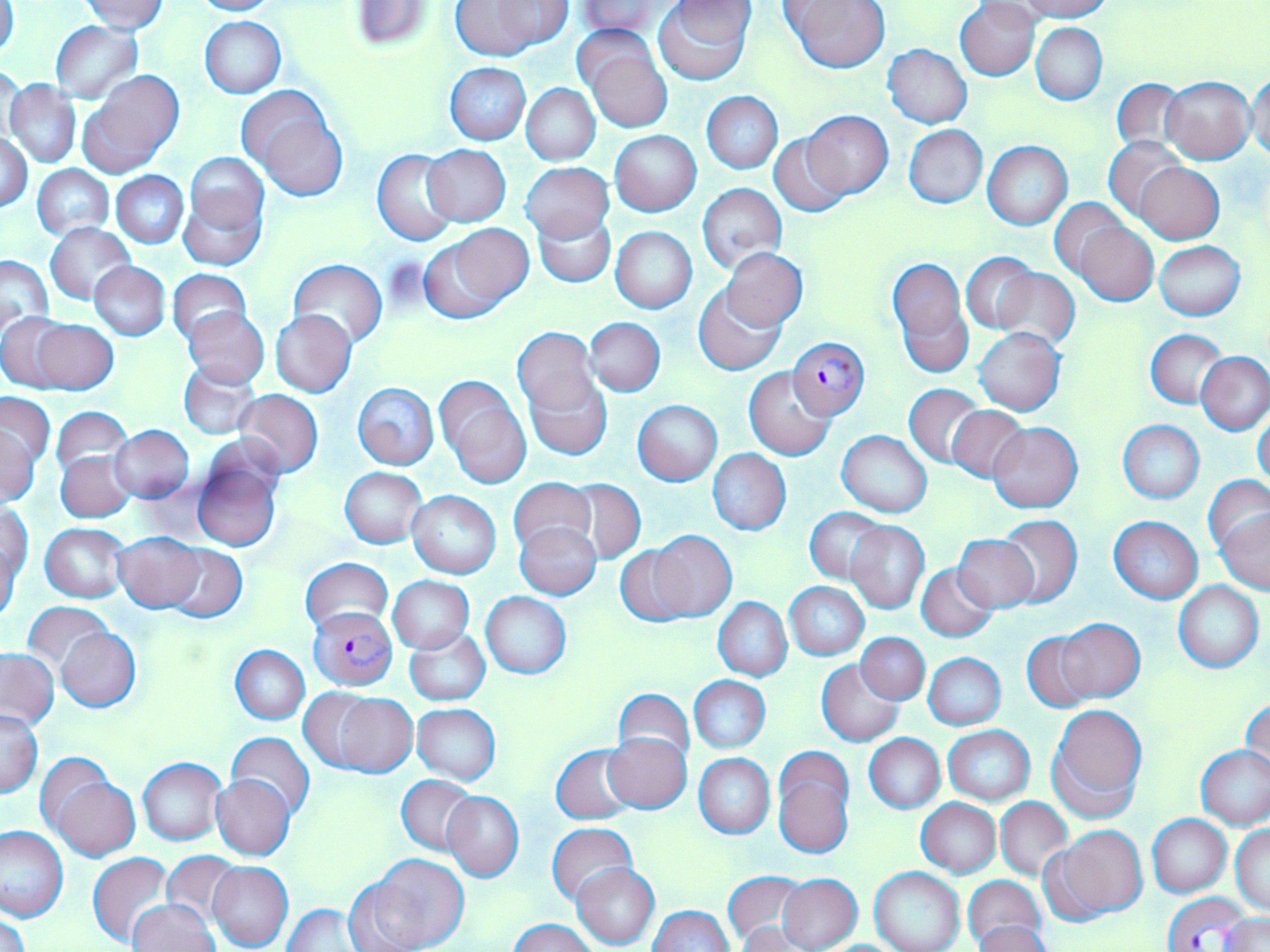
Summary:
  - Coordinate format: approximate bounding boxes as (x1, y1, x2, y2) in pixels
  - Uninfected red blood cell locations: (187, 0, 278, 16), (447, 0, 570, 60), (575, 0, 668, 38), (654, 0, 755, 86), (781, 0, 890, 72), (1017, 0, 1112, 21), (81, 1, 169, 35), (349, 1, 436, 50), (0, 2, 19, 62), (955, 2, 1040, 81), (199, 16, 286, 98), (51, 21, 142, 102), (1031, 22, 1107, 104), (583, 39, 675, 134), (883, 45, 971, 128), (445, 63, 531, 145), (1, 64, 25, 147), (78, 70, 183, 176), (1247, 72, 1270, 160), (1164, 76, 1253, 164), (1110, 77, 1188, 158), (5, 80, 82, 168), (520, 83, 600, 164), (237, 87, 344, 194), (702, 92, 782, 174), (803, 111, 893, 198), (904, 125, 988, 208), (610, 131, 701, 216), (1, 132, 32, 212), (769, 133, 854, 217), (904, 133, 1070, 216), (1105, 138, 1187, 223), (983, 142, 1071, 229), (422, 144, 511, 227), (373, 148, 460, 246), (185, 152, 268, 233), (521, 162, 613, 242), (1135, 162, 1223, 243), (32, 164, 115, 239), (112, 171, 188, 248), (698, 183, 786, 274), (178, 185, 266, 272), (1051, 198, 1133, 285), (534, 212, 614, 287), (1073, 219, 1158, 306), (45, 222, 136, 306), (419, 226, 532, 324), (611, 226, 698, 313), (1155, 241, 1246, 320), (720, 248, 807, 330), (962, 252, 1039, 333), (0, 254, 52, 336), (888, 258, 971, 377), (289, 259, 387, 348), (90, 262, 170, 341), (991, 267, 1078, 351), (167, 269, 252, 345), (694, 283, 786, 375), (183, 307, 268, 387), (271, 309, 357, 398), (2, 314, 73, 391), (27, 316, 118, 394), (584, 316, 665, 397), (975, 328, 1065, 416), (514, 329, 601, 425), (1147, 330, 1228, 408), (1197, 352, 1270, 434), (179, 361, 261, 439), (744, 366, 836, 460), (526, 371, 612, 460), (437, 377, 531, 490), (353, 382, 439, 470), (904, 384, 985, 469), (234, 389, 322, 478), (1, 393, 54, 474), (633, 400, 722, 485), (52, 407, 132, 481), (946, 407, 1029, 483), (1254, 410, 1270, 490), (1119, 419, 1204, 504), (1, 423, 41, 506), (989, 423, 1082, 514), (109, 425, 195, 503), (837, 430, 931, 517), (708, 448, 791, 536), (56, 450, 135, 522), (192, 458, 281, 552), (340, 466, 428, 547), (509, 476, 596, 559), (1205, 476, 1270, 557), (563, 481, 643, 563), (406, 490, 500, 578), (3, 503, 33, 590), (804, 506, 890, 584), (1216, 507, 1269, 595), (994, 515, 1081, 607), (1110, 517, 1202, 602), (845, 521, 928, 613), (514, 522, 601, 600), (40, 523, 131, 603), (647, 531, 735, 621), (113, 532, 203, 611), (952, 534, 1040, 612), (1, 540, 23, 626), (615, 541, 703, 627), (160, 542, 247, 624), (300, 557, 393, 636), (917, 562, 997, 642), (389, 576, 474, 655), (785, 582, 868, 660), (1174, 582, 1263, 672), (480, 592, 572, 678), (713, 597, 791, 682), (23, 602, 114, 673), (1055, 618, 1143, 702), (56, 628, 139, 711), (404, 628, 490, 706), (1022, 629, 1101, 711), (857, 633, 929, 703), (231, 646, 309, 725), (858, 646, 1003, 718), (0, 649, 58, 730), (932, 651, 1014, 807), (924, 654, 1004, 729), (817, 659, 904, 746), (689, 676, 770, 753), (305, 688, 417, 777), (614, 689, 694, 772), (1240, 696, 1269, 783), (412, 704, 501, 784), (1047, 704, 1146, 817), (1, 708, 42, 797), (942, 725, 1034, 806), (226, 732, 313, 818), (603, 733, 691, 814), (863, 733, 945, 813), (551, 744, 640, 824), (1195, 745, 1270, 831), (694, 753, 774, 839), (772, 753, 854, 858), (137, 756, 227, 846), (43, 769, 140, 862), (212, 775, 296, 860), (396, 775, 480, 856), (442, 791, 523, 881), (995, 798, 1071, 882), (915, 799, 1001, 877), (1147, 815, 1231, 897), (547, 823, 638, 908), (1231, 824, 1269, 913), (0, 825, 68, 922), (1046, 825, 1146, 921), (160, 851, 244, 927), (87, 852, 176, 949), (358, 853, 470, 952), (208, 861, 293, 951), (573, 863, 659, 950), (869, 867, 965, 952), (723, 870, 810, 948), (777, 874, 862, 952), (962, 876, 1046, 951), (128, 900, 220, 952), (282, 903, 370, 951), (647, 905, 735, 952), (1, 912, 29, 952), (1219, 915, 1269, 951), (510, 918, 596, 952), (973, 922, 1053, 952)
  - Plasmodium falciparum-infected red blood cell locations: (789, 338, 870, 420), (309, 609, 398, 690), (1164, 893, 1250, 951)
  - Slide-level diagnosis: Plasmodium falciparum
  - Modality: light microscopy
  - Stain: May-Grünwald-Giemsa
  - Field of view: single
  - Image size: 1270×952 pixels
  - Magnification: 1000x
  - Preparation: thin blood smear